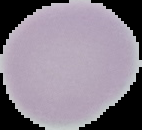
image type = segmented cell region with the area outside set to black
image size = 142×130 pixels
preparation = thin blood film
malaria status = uninfected